Classify this cell by malaria status.
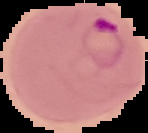

Parasitized.

Summary:
  - Image size: 148×133 pixels
  - Image type: segmented cell region on a black background
  - Preparation: thin blood film